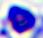 A leukocyte is seen. Photomicrograph. 400x magnification.